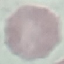
malaria_status: uninfected
capture: smartphone through the microscope eyepiece
image_type: automatically extracted cell patch, resized to 64 × 64 pixels
stain: Giemsa
preparation: thin smear